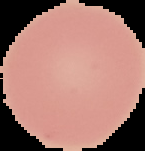

{
  "image_size": "145×151 pixels",
  "image_type": "segmented cell region on a black background",
  "preparation": "thin blood film",
  "result": "no Plasmodium parasites seen"
}